Identify the blood parasite species.
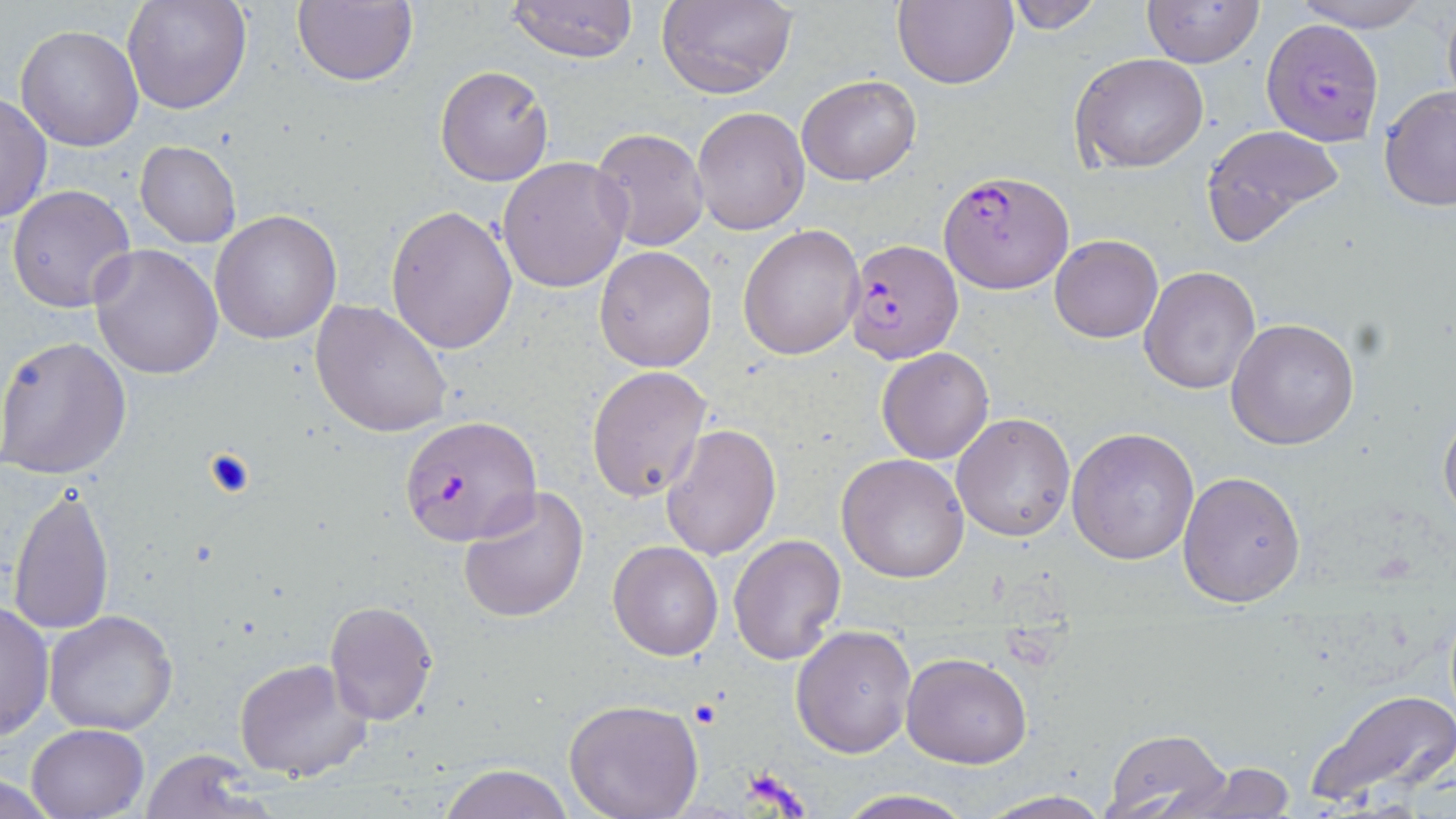

Plasmodium falciparum.

Summary:
  - Coordinate format: approximate bounding boxes as (x1, y1, x2, y2) in pixels
  - Plasmodium falciparum-infected red blood cell locations: (1261, 18, 1387, 148), (940, 170, 1075, 294), (844, 237, 963, 365), (400, 413, 541, 547)
  - Uninfected red blood cell locations: (123, 0, 252, 114), (293, 0, 418, 86), (894, 0, 1019, 89), (999, 0, 1104, 34), (1142, 0, 1263, 68), (1288, 0, 1436, 32), (504, 1, 639, 63), (656, 1, 797, 98), (1441, 2, 1456, 118), (14, 26, 144, 151), (1069, 52, 1209, 174), (435, 65, 554, 185), (797, 74, 921, 186), (1379, 86, 1456, 211), (0, 95, 52, 225), (692, 107, 810, 234), (1201, 123, 1346, 244), (589, 126, 709, 251), (135, 140, 241, 250), (496, 157, 632, 293), (7, 184, 136, 313), (386, 205, 517, 355), (211, 209, 343, 344), (738, 224, 865, 360), (1050, 234, 1162, 343), (89, 243, 223, 380), (593, 245, 717, 371), (1138, 265, 1261, 397), (310, 299, 453, 439), (1227, 316, 1360, 450), (0, 333, 132, 479), (877, 347, 994, 464), (587, 365, 713, 503), (1439, 402, 1456, 526), (950, 412, 1075, 542), (660, 425, 782, 561), (1068, 425, 1200, 566), (836, 453, 970, 584), (1176, 470, 1307, 609), (7, 482, 115, 637), (457, 486, 589, 624), (728, 534, 848, 666), (607, 541, 723, 660), (0, 599, 53, 743), (324, 602, 438, 725), (45, 609, 178, 735), (790, 624, 916, 758), (902, 653, 1033, 768), (234, 658, 372, 783), (1304, 689, 1456, 810), (563, 698, 704, 819), (27, 724, 147, 818), (1099, 728, 1233, 818), (135, 750, 268, 819), (1166, 762, 1300, 817), (438, 765, 573, 819), (1, 777, 62, 817), (829, 791, 982, 819), (974, 791, 1120, 819)
  - Preparation: thin blood film
  - Field of view: one of a larger specimen
  - Magnification: 1000x
  - Stain: May-Grünwald-Giemsa
  - Modality: light microscopy
  - Image size: 1456×819 pixels